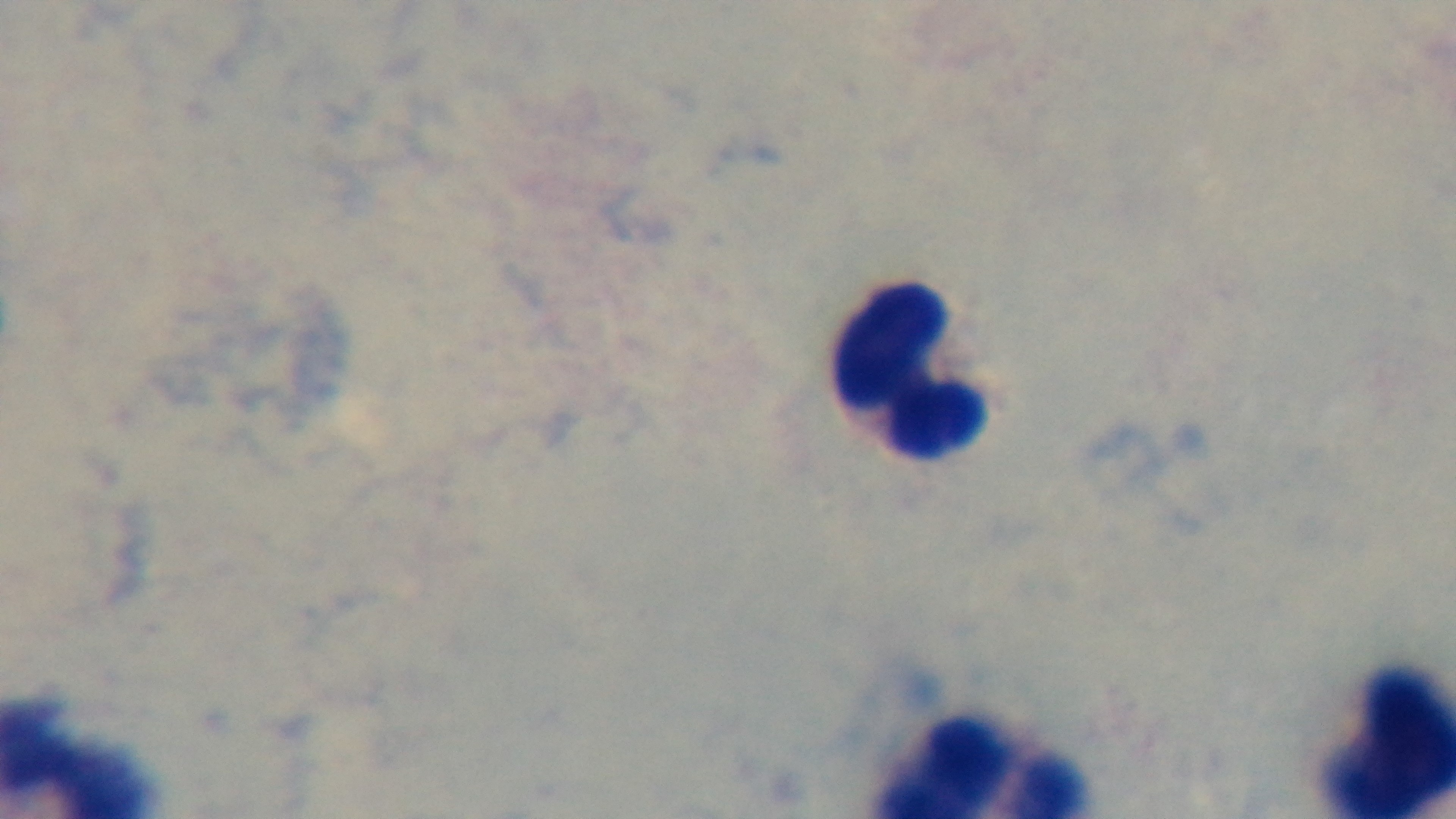
Giemsa-stained. One field from the slide. Captured with a mounted 4K digital camera. 100x oil-immersion objective. Photomicrograph. Malaria status: uninfected. Preparation: thick blood film.